Comment on the morphology of the red blood cells.
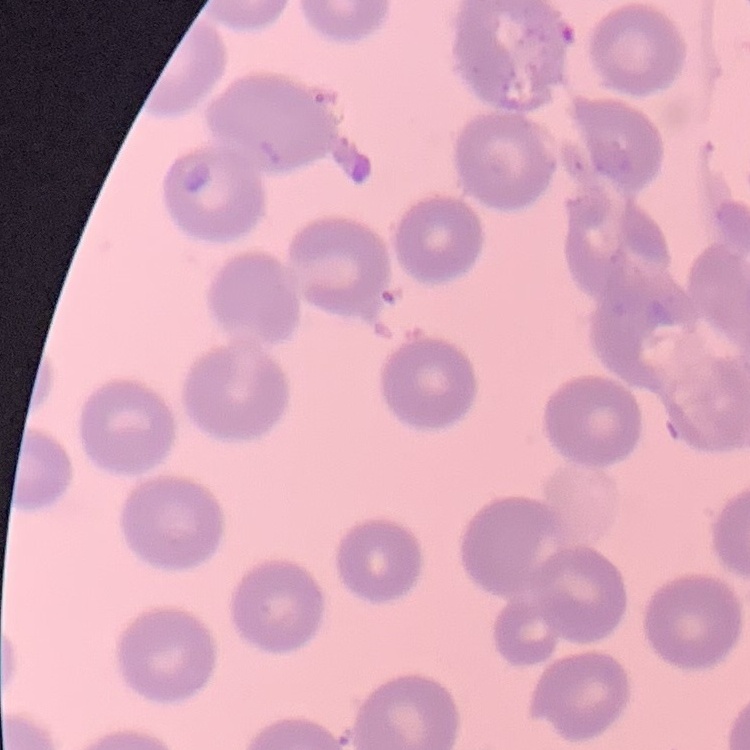
No rouleaux formation.

{
  "preparation": "thin peripheral smear",
  "image_type": "one tile cut from a larger photomicrograph",
  "stain": "Field's or Giemsa"
}